Outline each Plasmodium falciparum-infected red blood cell.
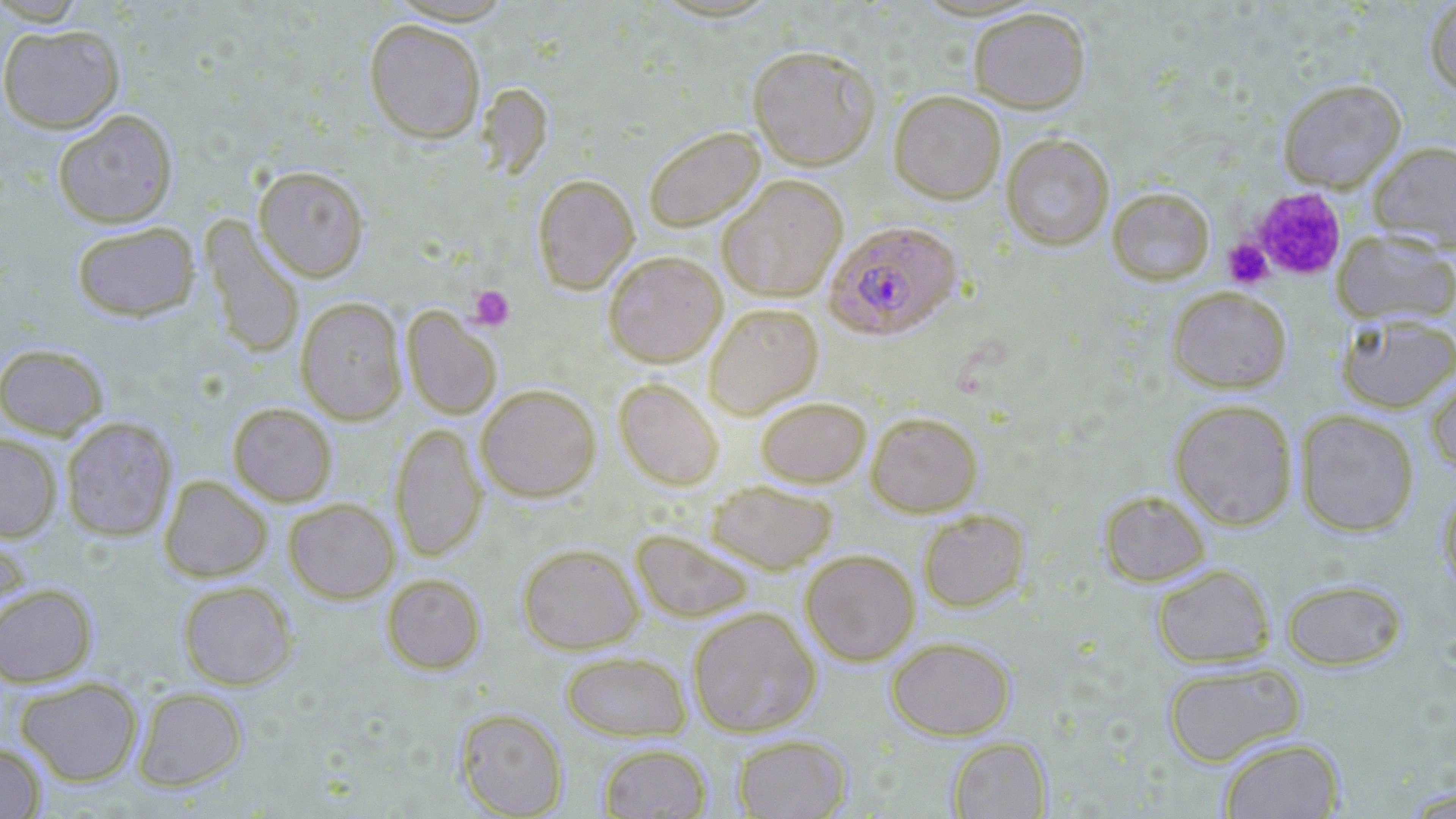

Approximate bounding boxes as named x1/y1/x2/y2 corners in pixels.
Plasmodium falciparum-infected red blood cells: (x1=824, y1=220, x2=962, y2=340).

slide-level diagnosis = Plasmodium falciparum
platelet locations = approximate bounding boxes as named x1/y1/x2/y2 corners in pixels: (x1=1247, y1=186, x2=1348, y2=281), (x1=1223, y1=238, x2=1273, y2=289), (x1=467, y1=285, x2=514, y2=330)
uninfected red blood cell locations = approximate bounding boxes as named x1/y1/x2/y2 corners in pixels: (x1=1424, y1=0, x2=1456, y2=96), (x1=967, y1=6, x2=1091, y2=113), (x1=364, y1=18, x2=486, y2=143), (x1=0, y1=24, x2=124, y2=133), (x1=746, y1=44, x2=880, y2=170), (x1=1278, y1=78, x2=1406, y2=192), (x1=478, y1=82, x2=553, y2=181), (x1=889, y1=90, x2=1006, y2=204), (x1=53, y1=110, x2=178, y2=228), (x1=643, y1=126, x2=765, y2=232), (x1=1001, y1=133, x2=1114, y2=251), (x1=1368, y1=141, x2=1456, y2=251), (x1=253, y1=165, x2=370, y2=282), (x1=532, y1=174, x2=639, y2=294), (x1=717, y1=174, x2=848, y2=302), (x1=1107, y1=187, x2=1215, y2=285), (x1=201, y1=218, x2=305, y2=359), (x1=71, y1=221, x2=200, y2=322), (x1=1332, y1=230, x2=1456, y2=325), (x1=603, y1=250, x2=727, y2=367), (x1=1166, y1=286, x2=1292, y2=393), (x1=295, y1=296, x2=407, y2=425), (x1=704, y1=303, x2=823, y2=418), (x1=402, y1=306, x2=502, y2=419), (x1=1335, y1=311, x2=1456, y2=414), (x1=0, y1=343, x2=109, y2=439), (x1=1425, y1=370, x2=1456, y2=480), (x1=613, y1=378, x2=724, y2=490), (x1=476, y1=384, x2=601, y2=501), (x1=755, y1=396, x2=871, y2=487), (x1=1169, y1=398, x2=1298, y2=530), (x1=227, y1=402, x2=337, y2=506), (x1=1295, y1=409, x2=1419, y2=537), (x1=866, y1=411, x2=982, y2=516), (x1=60, y1=416, x2=177, y2=542), (x1=390, y1=423, x2=486, y2=562), (x1=0, y1=433, x2=63, y2=541), (x1=159, y1=475, x2=272, y2=582), (x1=707, y1=480, x2=838, y2=574), (x1=1437, y1=483, x2=1456, y2=600), (x1=1098, y1=489, x2=1211, y2=587), (x1=283, y1=498, x2=399, y2=603), (x1=918, y1=509, x2=1030, y2=612), (x1=0, y1=526, x2=32, y2=629), (x1=630, y1=529, x2=756, y2=623), (x1=517, y1=543, x2=643, y2=654), (x1=800, y1=549, x2=920, y2=666), (x1=1151, y1=563, x2=1275, y2=668), (x1=381, y1=572, x2=486, y2=674), (x1=1280, y1=577, x2=1407, y2=671), (x1=177, y1=580, x2=298, y2=690), (x1=0, y1=583, x2=97, y2=688), (x1=688, y1=606, x2=821, y2=737), (x1=886, y1=635, x2=1016, y2=740), (x1=560, y1=651, x2=692, y2=741), (x1=1161, y1=661, x2=1305, y2=767), (x1=15, y1=676, x2=143, y2=786), (x1=132, y1=686, x2=248, y2=792), (x1=455, y1=708, x2=568, y2=818), (x1=732, y1=734, x2=852, y2=818), (x1=947, y1=736, x2=1051, y2=818), (x1=1218, y1=736, x2=1345, y2=818), (x1=0, y1=742, x2=47, y2=819), (x1=597, y1=742, x2=712, y2=818)
field of view = single
preparation = thin blood film
modality = light microscopy
magnification = 1000x
stain = May-Grünwald-Giemsa
image size = 1456×819 pixels